Outline each uninfected red blood cell.
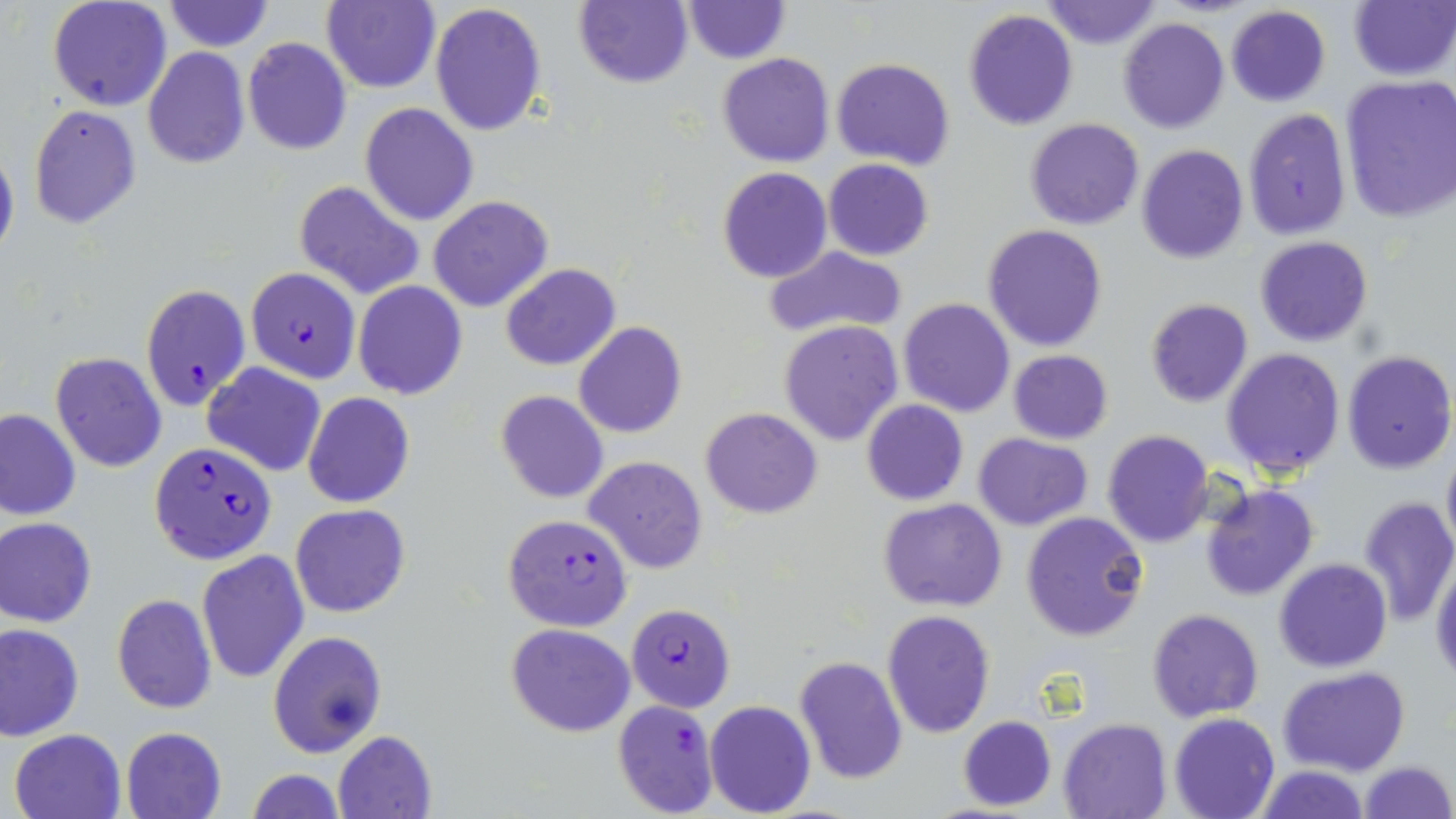
Approximate bounding boxes as (x1,y1)-(x2,y2) corner pairs in pixels.
Uninfected red blood cells: (47,0)-(172,113), (322,0)-(440,93), (573,0)-(693,89), (1041,0)-(1162,50), (1349,0)-(1456,82), (164,1)-(273,51), (681,1)-(789,64), (430,2)-(548,139), (1225,6)-(1330,107), (964,8)-(1078,130), (1118,16)-(1230,133), (243,38)-(351,154), (143,47)-(250,169), (717,52)-(834,167), (832,58)-(956,168), (1338,73)-(1456,222), (360,102)-(480,225), (28,105)-(143,231), (1243,108)-(1352,242), (1025,117)-(1145,231), (0,142)-(19,269), (1136,145)-(1249,264), (824,158)-(933,260), (718,166)-(832,283), (293,180)-(425,300), (428,195)-(555,313), (982,225)-(1108,351), (1255,236)-(1373,348), (761,245)-(907,342), (500,264)-(621,370), (352,280)-(467,400), (898,298)-(1015,418), (1145,298)-(1253,407), (780,319)-(904,447), (574,321)-(686,439), (1221,348)-(1346,477), (1008,350)-(1113,443), (1342,350)-(1455,473), (51,352)-(166,472), (201,362)-(326,476), (496,391)-(609,505), (303,393)-(414,508), (861,398)-(968,506), (0,407)-(81,521), (699,407)-(823,518), (1102,430)-(1214,548), (973,432)-(1092,530), (1441,444)-(1456,558), (585,456)-(708,573), (1200,483)-(1319,601), (1357,496)-(1456,626), (878,498)-(1007,611), (291,504)-(410,617), (1021,512)-(1150,642), (0,517)-(96,628), (196,549)-(309,686), (1431,557)-(1456,685), (1273,558)-(1393,673), (112,593)-(218,713), (1147,608)-(1263,722), (881,611)-(996,738), (0,622)-(84,740), (505,623)-(635,737), (268,630)-(387,757), (793,656)-(907,786), (1279,667)-(1409,776), (704,700)-(816,818), (1169,713)-(1279,819), (957,716)-(1056,811), (1058,717)-(1172,819), (121,726)-(227,819), (9,728)-(127,819), (333,730)-(436,817), (1359,760)-(1452,818), (1255,765)-(1369,819), (244,770)-(347,818).

slide-level diagnosis = Plasmodium falciparum
image size = 1456×819 pixels
Plasmodium falciparum-infected red blood cell locations = approximate bounding boxes as (x1,y1)-(x2,y2) corner pairs in pixels: (246,267)-(360,383), (141,283)-(250,410), (149,441)-(276,565), (502,513)-(633,632), (626,603)-(735,711), (611,699)-(719,817)
magnification = 1000x
modality = light microscopy
preparation = thin blood smear
stain = May-Grünwald-Giemsa
field of view = single